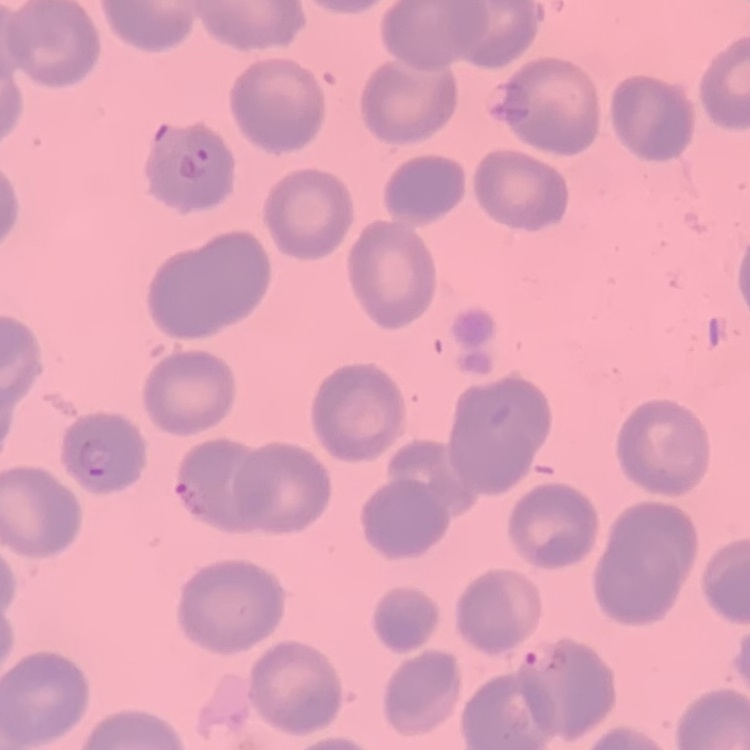
erythrocyte_morphology: no rouleaux formation
preparation: thin peripheral smear
image_type: square crop of a larger photomicrograph
stain: Field's or Giemsa